Outline each blood parasite and name the species.
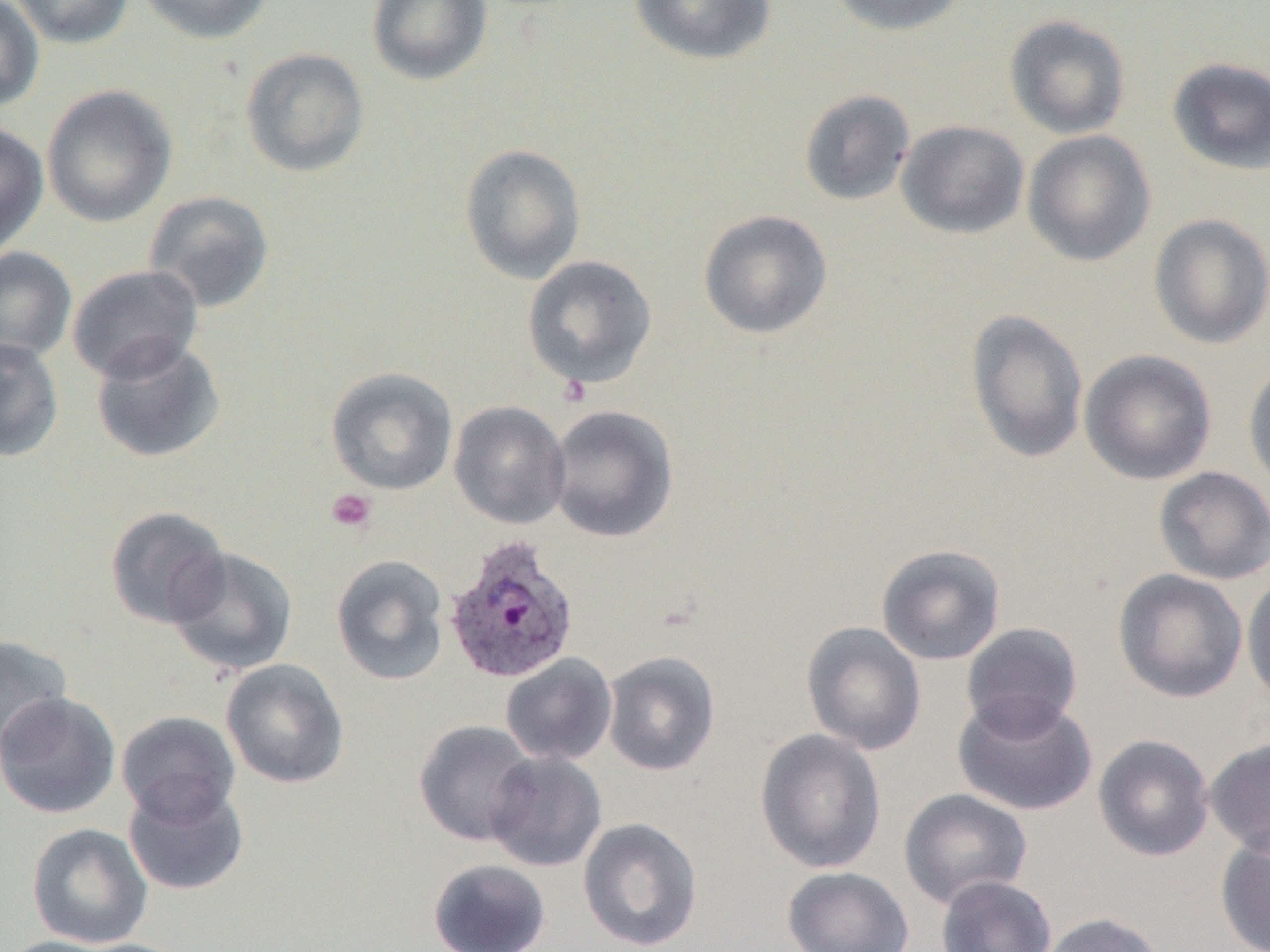

Approximate bounding boxes as named x1/y1/x2/y2 corners in pixels.
Plasmodium ovale-infected red blood cells: (x1=443, y1=535, x2=580, y2=684).
No Plasmodium falciparum, Plasmodium malariae, Plasmodium vivax, Babesia divergens, or Trypanosoma brucei observed.

Summary:
  - Platelet locations: (x1=326, y1=488, x2=377, y2=532)
  - Uninfected red blood cell locations: (x1=0, y1=0, x2=45, y2=113), (x1=10, y1=0, x2=134, y2=49), (x1=137, y1=0, x2=274, y2=45), (x1=366, y1=0, x2=493, y2=87), (x1=628, y1=0, x2=777, y2=65), (x1=824, y1=0, x2=969, y2=36), (x1=1004, y1=14, x2=1131, y2=140), (x1=240, y1=47, x2=370, y2=177), (x1=1167, y1=57, x2=1270, y2=175), (x1=41, y1=84, x2=177, y2=228), (x1=798, y1=89, x2=915, y2=206), (x1=896, y1=119, x2=1029, y2=240), (x1=0, y1=121, x2=49, y2=255), (x1=1022, y1=130, x2=1156, y2=266), (x1=459, y1=143, x2=587, y2=284), (x1=143, y1=191, x2=275, y2=314), (x1=698, y1=209, x2=833, y2=339), (x1=1148, y1=213, x2=1270, y2=349), (x1=0, y1=246, x2=77, y2=365), (x1=521, y1=255, x2=657, y2=389), (x1=67, y1=264, x2=204, y2=382), (x1=965, y1=309, x2=1090, y2=464), (x1=90, y1=336, x2=227, y2=463), (x1=0, y1=337, x2=64, y2=462), (x1=1079, y1=349, x2=1217, y2=485), (x1=1243, y1=357, x2=1270, y2=494), (x1=326, y1=366, x2=459, y2=496), (x1=449, y1=400, x2=571, y2=529), (x1=548, y1=404, x2=679, y2=542), (x1=1153, y1=466, x2=1270, y2=585), (x1=105, y1=505, x2=231, y2=629), (x1=876, y1=544, x2=1007, y2=666), (x1=165, y1=547, x2=298, y2=678), (x1=331, y1=554, x2=449, y2=686), (x1=1112, y1=569, x2=1248, y2=703), (x1=1242, y1=570, x2=1270, y2=708), (x1=801, y1=621, x2=927, y2=755), (x1=961, y1=622, x2=1083, y2=735), (x1=0, y1=634, x2=74, y2=758), (x1=602, y1=651, x2=721, y2=776), (x1=500, y1=654, x2=618, y2=766), (x1=220, y1=659, x2=350, y2=789), (x1=0, y1=691, x2=121, y2=819), (x1=953, y1=692, x2=1099, y2=816), (x1=116, y1=711, x2=241, y2=825), (x1=413, y1=719, x2=539, y2=847), (x1=755, y1=728, x2=887, y2=874), (x1=1093, y1=734, x2=1215, y2=861), (x1=1204, y1=738, x2=1270, y2=856), (x1=485, y1=751, x2=608, y2=872), (x1=123, y1=778, x2=250, y2=896), (x1=899, y1=788, x2=1033, y2=910), (x1=578, y1=817, x2=703, y2=951), (x1=26, y1=822, x2=153, y2=948), (x1=1216, y1=827, x2=1270, y2=952), (x1=427, y1=858, x2=552, y2=952), (x1=782, y1=866, x2=915, y2=952), (x1=936, y1=874, x2=1057, y2=952), (x1=1038, y1=912, x2=1167, y2=952), (x1=0, y1=935, x2=125, y2=952), (x1=65, y1=938, x2=197, y2=952)
  - Slide-level diagnosis: Plasmodium ovale
  - Image size: 1270×952 pixels
  - Magnification: 1000x
  - Modality: light microscopy
  - Field of view: single
  - Preparation: thin blood film